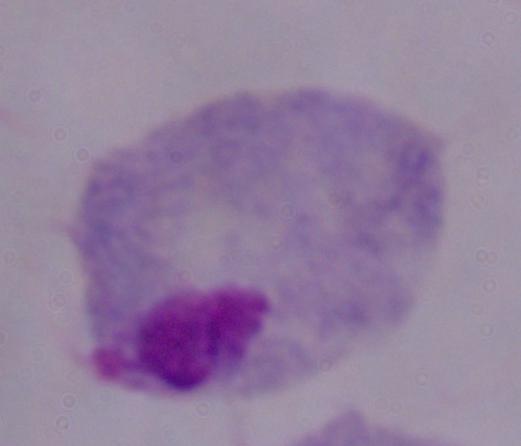
Summary:
  - Magnification: 1000x
  - Identification: trichomonad
  - Modality: micrograph